Locate and identify every blood parasite.
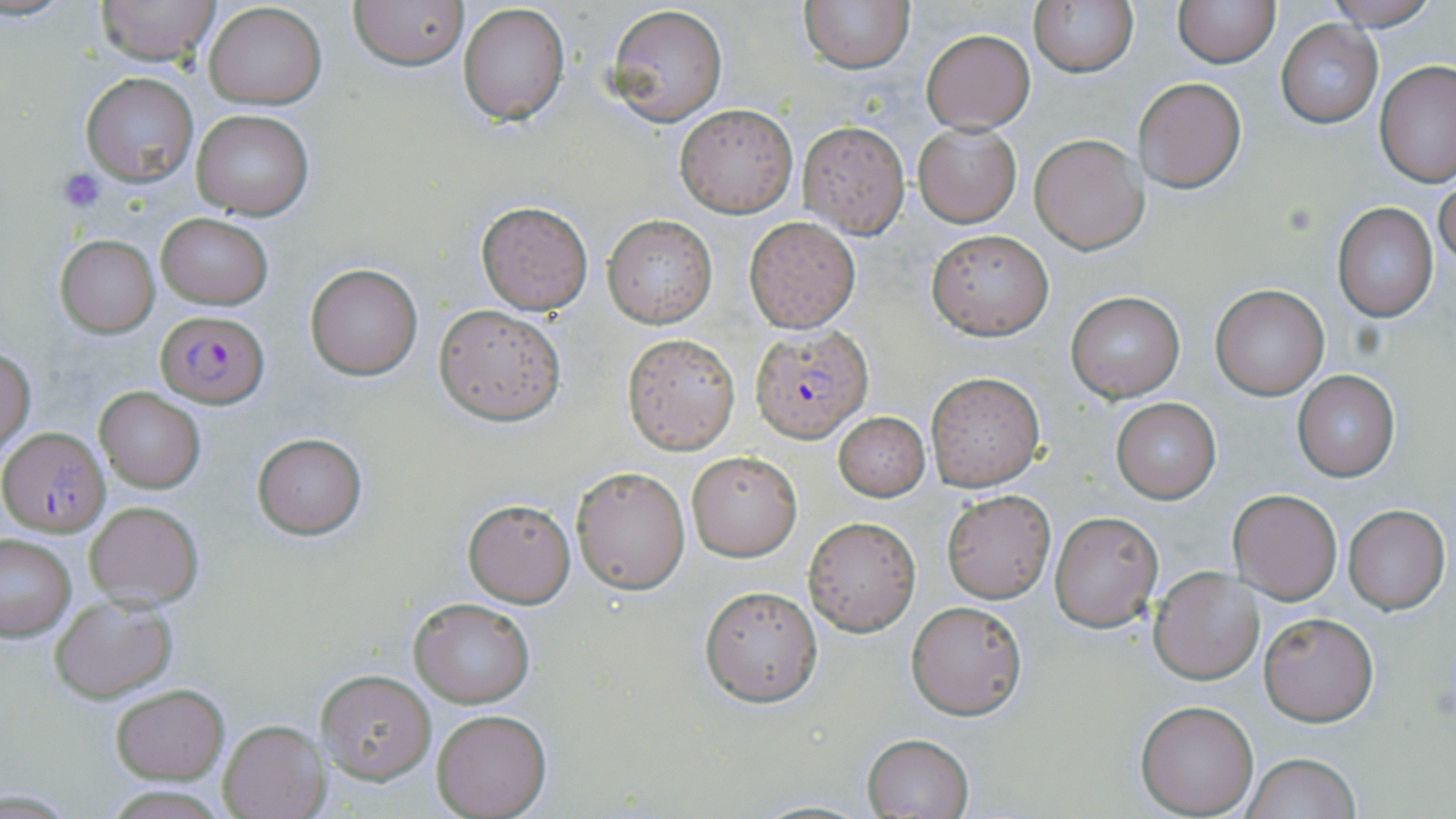

Approximate bounding boxes as (x1, y1, x2, y2) in pixels.
Plasmodium falciparum-infected red blood cells: (155, 311, 268, 405), (749, 327, 872, 443), (1, 425, 108, 537).
No Plasmodium ovale, Plasmodium malariae, Plasmodium vivax, Babesia divergens, or Trypanosoma brucei observed.

{
  "slide_level_diagnosis": "Plasmodium falciparum",
  "image_size": "1456×819 pixels",
  "stain": "May-Grünwald-Giemsa",
  "magnification": "1000x",
  "uninfected_red_blood_cell_locations": "approximate bounding boxes as (x1, y1, x2, y2) in pixels: (96, 0, 221, 66), (349, 0, 468, 72), (799, 0, 913, 72), (1029, 0, 1137, 79), (1172, 0, 1280, 67), (1325, 0, 1442, 31), (203, 2, 326, 109), (457, 3, 570, 126), (605, 4, 728, 127), (1276, 20, 1383, 128), (920, 28, 1035, 133), (1375, 60, 1454, 189), (81, 72, 200, 188), (1134, 77, 1246, 193), (674, 103, 798, 218), (192, 109, 315, 222), (796, 120, 911, 238), (914, 122, 1021, 227), (1030, 134, 1148, 255), (1434, 177, 1456, 267), (476, 200, 594, 315), (1332, 202, 1438, 321), (155, 212, 272, 309), (602, 213, 717, 329), (744, 216, 861, 333), (927, 230, 1052, 339), (56, 235, 159, 336), (305, 264, 422, 380), (1210, 282, 1329, 400), (1065, 290, 1186, 404), (434, 304, 565, 424), (624, 332, 741, 454), (1, 348, 36, 453), (1292, 370, 1400, 481), (926, 372, 1044, 491), (96, 389, 204, 492), (1111, 397, 1221, 503), (833, 411, 931, 501), (252, 432, 367, 538), (686, 450, 801, 560), (570, 465, 689, 594), (1230, 488, 1342, 603), (942, 491, 1055, 603), (463, 498, 576, 606), (83, 499, 204, 607), (1343, 504, 1449, 613), (1050, 511, 1162, 632), (804, 515, 921, 636), (0, 534, 77, 641), (1150, 566, 1263, 685), (699, 585, 823, 707), (49, 594, 178, 703), (410, 598, 534, 707), (905, 601, 1027, 720), (1257, 610, 1380, 726), (317, 668, 436, 783), (110, 684, 229, 783), (1136, 699, 1259, 816), (431, 710, 552, 818), (217, 719, 328, 819), (862, 733, 974, 819), (1242, 753, 1359, 819), (103, 784, 232, 818)",
  "preparation": "thin blood film",
  "field_of_view": "single",
  "platelet_locations": "approximate bounding boxes as (x1, y1, x2, y2) in pixels: (56, 168, 106, 213)",
  "modality": "light microscopy"
}